Report the malaria status of this cell.
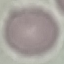
Uninfected.

image type = automatically extracted cell patch, resized to 64 × 64 pixels
capture = smartphone camera at the microscope eyepiece
preparation = thin blood film
stain = Giemsa